Describe the morphology of the erythrocytes.
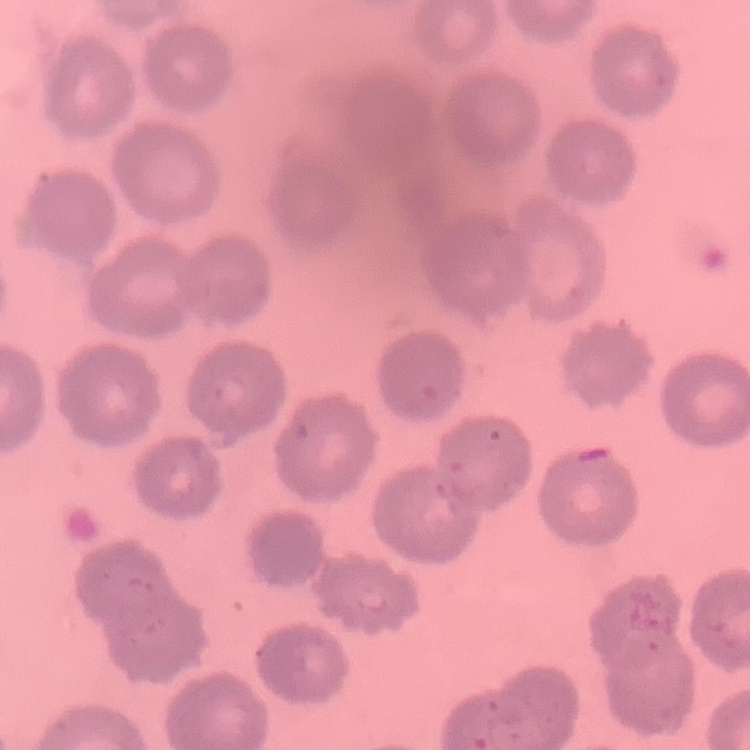
No rouleaux formation.

Summary:
  - Preparation: thin blood smear
  - Stain: Field's or Giemsa
  - Image type: square crop of a larger photomicrograph